Classify this cell by malaria status.
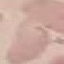

Uninfected.

Cell patch, automatically extracted from a larger field of view and resized to 64 × 64 pixels. Giemsa-stained preparation. Thin blood smear. Photographed with a smartphone camera at the microscope eyepiece.